Locate every leukocyte (white blood cell).
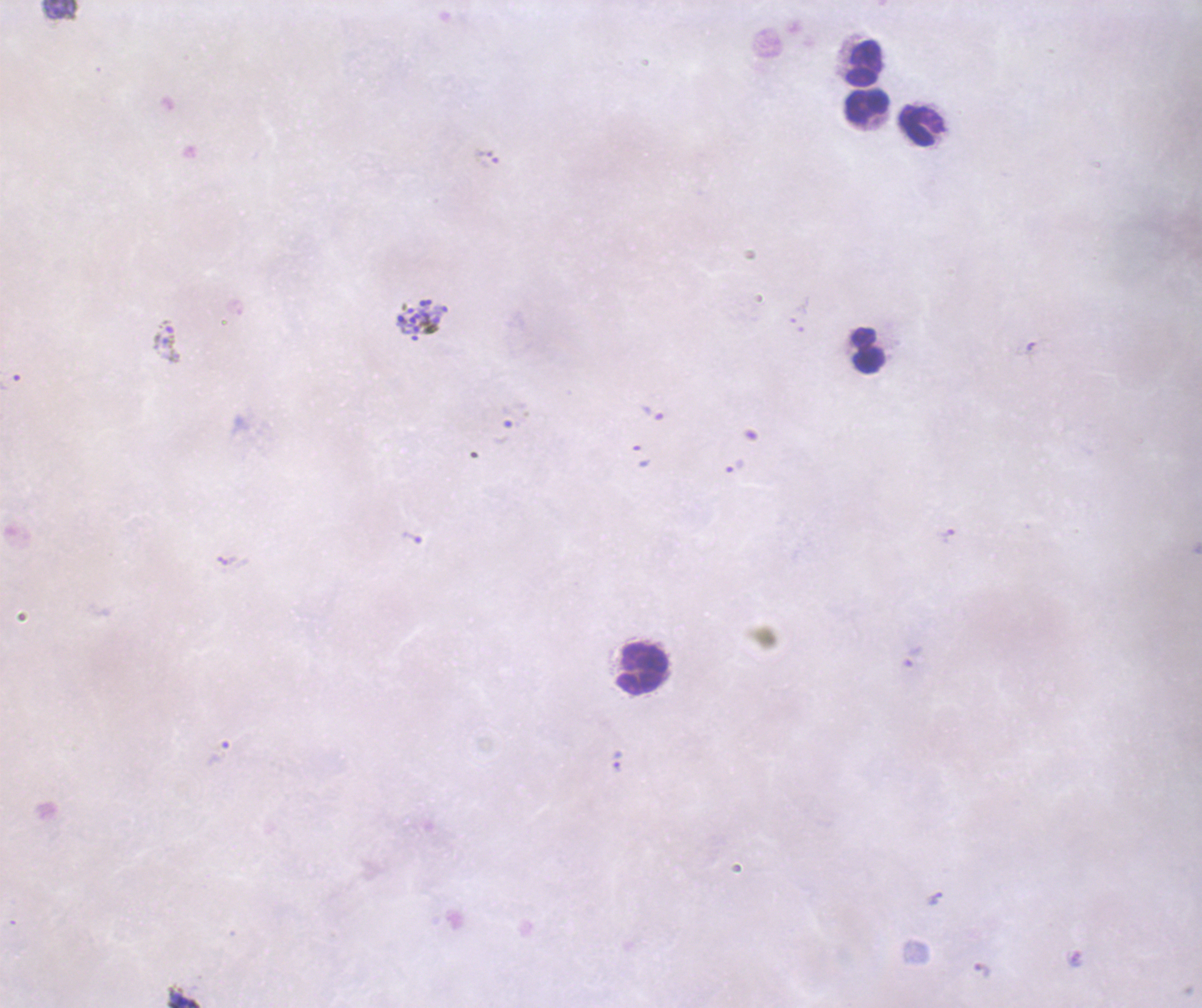
Approximate centers as [x, y] in pixels.
Leukocytes: [864, 64], [867, 108], [921, 127], [867, 351], [643, 667].

Approximate centers as [x, y] in pixels.
Summary:
  - Schizont locations: [422, 321]
  - Trophozoite locations: [167, 340], [653, 413], [735, 466], [948, 536], [412, 537], [617, 760]
  - Life-cycle stages observed: trophozoite, schizont
  - Preparation: thick smear of blood
  - Background quality: unsatisfactory
  - Stain: Romanowsky
  - Context: previously used in a real diagnosis
  - Image size: 1202×1008 pixels
  - Magnification: 100x
  - Coloration quality: bad
  - Field of view: single
  - Result: malaria parasites detected